Identify the cell.
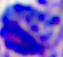

This is a leukocyte.

magnification: 400x
modality: photomicrograph